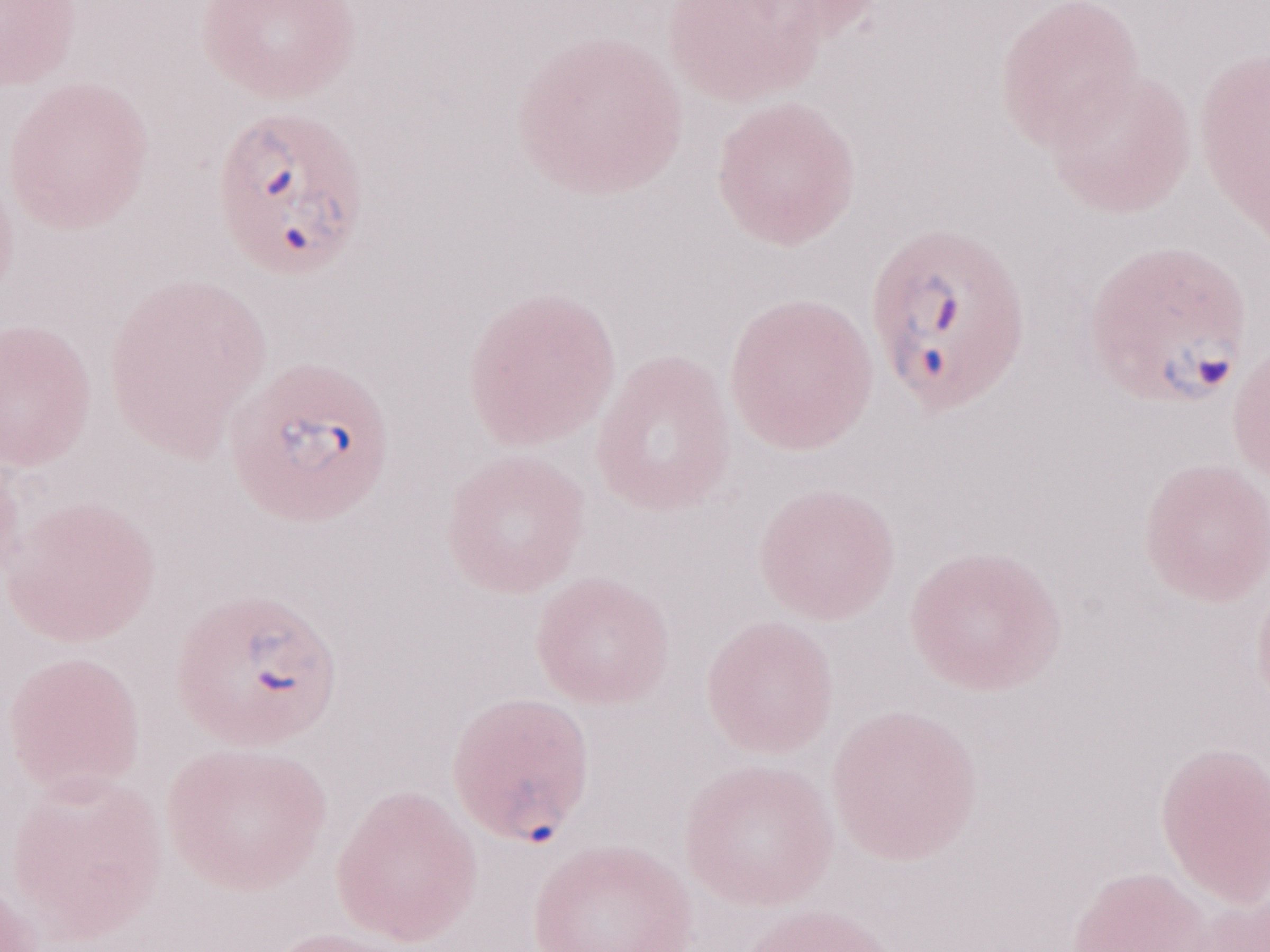

Image is 1270×952 pixels. Olympus BX43 microscope and DP73 digital camera. Thin blood film. Patient diagnosis: malaria infection. 1,000x magnification. May-Grünwald-Giemsa stain. One field of this slide.